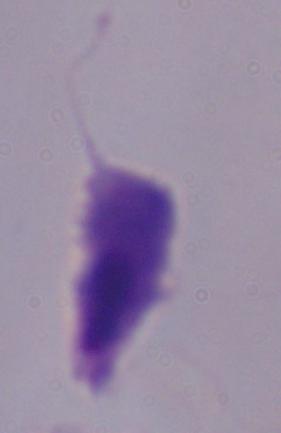

Summary:
  - Modality: photomicrograph
  - Identification: trichomonad
  - Magnification: 1000x